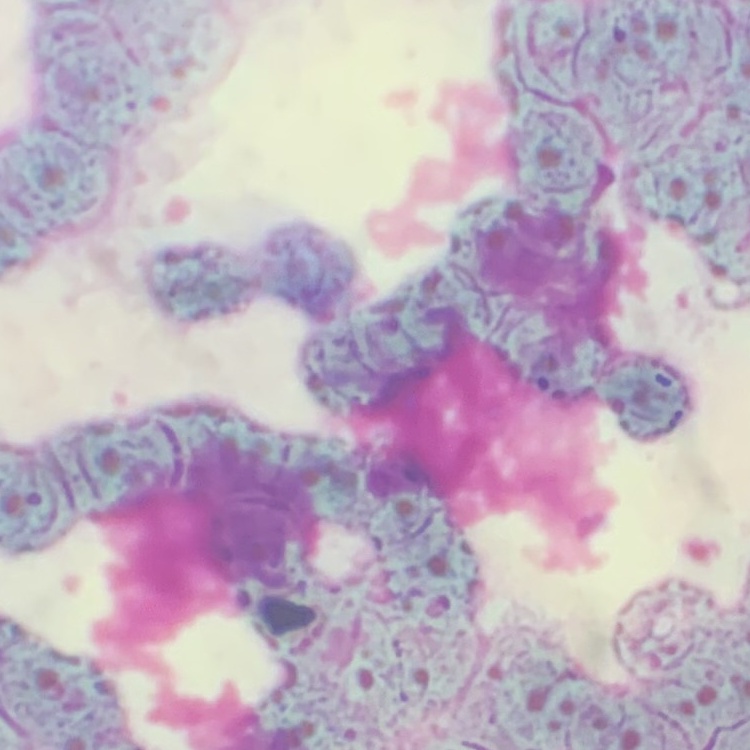 The red blood cells show rouleaux formation. Field's or Giemsa stain. Square crop of a larger photomicrograph. Thin blood film.